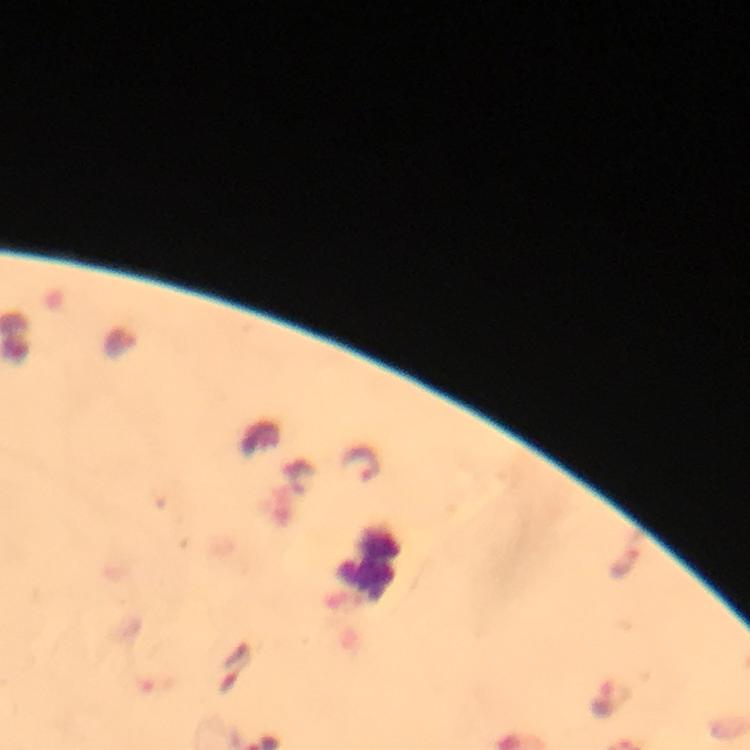 Approximate centers as (x, y) in pixels. Plasmodium parasite locations: (362, 464). Immersion oil was used. 100x magnification. Thick blood smear. Photographed with a smartphone mounted on the microscope. From a diagnostic examination for malaria. Cropped region of a single field of view. Image is 750×750 pixels. Giemsa stain.